Outline each blood parasite and name the species.
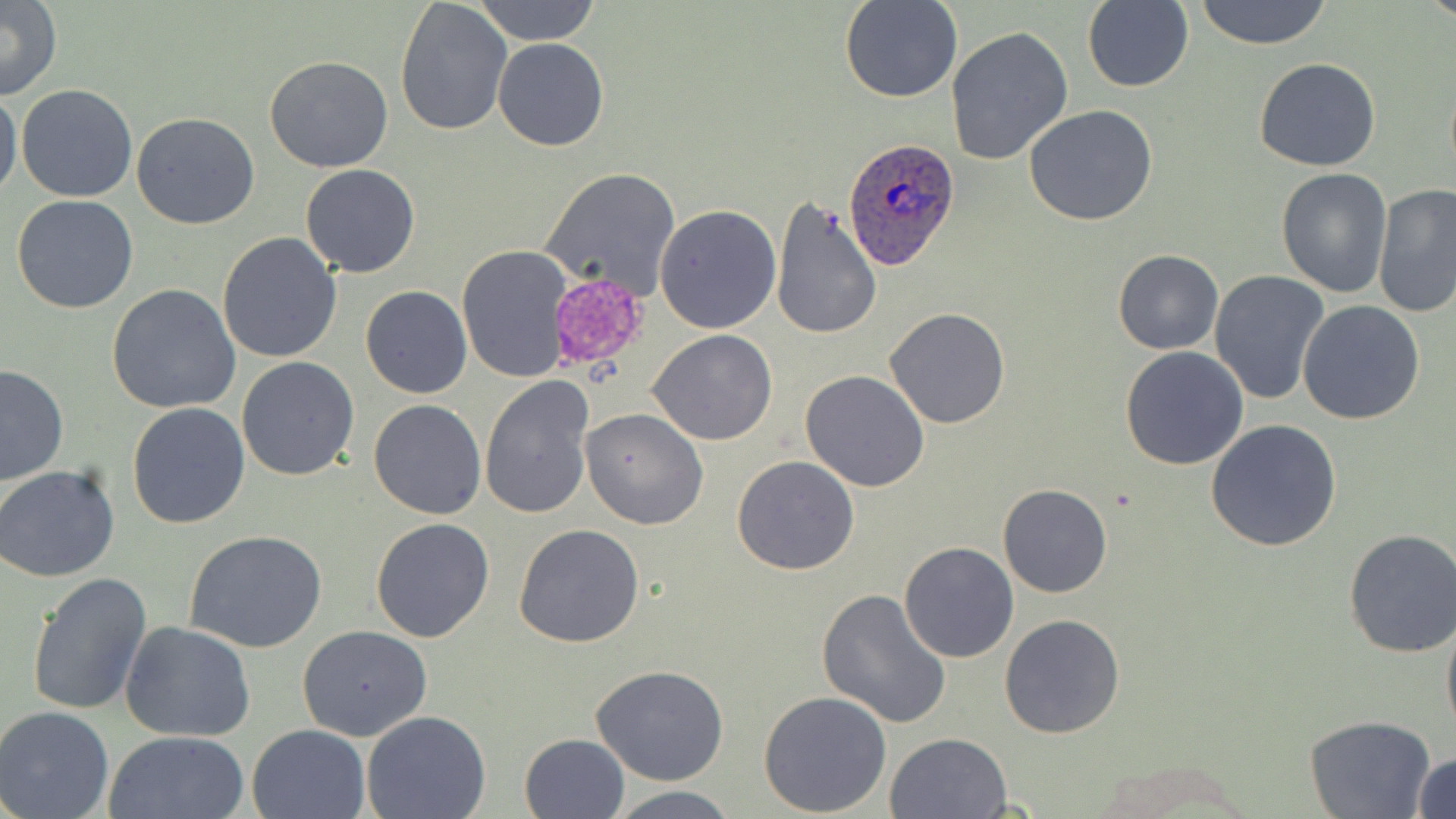

Approximate bounding boxes as (x1, y1, x2, y2) in pixels.
Plasmodium ovale-infected red blood cells: (844, 139, 959, 272).
No Plasmodium falciparum, Plasmodium malariae, Plasmodium vivax, Babesia divergens, or Trypanosoma brucei observed.

slide-level diagnosis = Plasmodium ovale
preparation = thin blood smear
modality = optical microscopy
image size = 1456×819 pixels
uninfected red blood cell locations = approximate bounding boxes as (x1, y1, x2, y2) in pixels: (473, 0, 602, 46), (839, 0, 962, 103), (1193, 0, 1333, 49), (0, 1, 62, 100), (393, 1, 512, 137), (1082, 1, 1195, 93), (946, 25, 1074, 167), (492, 38, 609, 151), (263, 55, 395, 173), (1254, 57, 1382, 171), (15, 84, 139, 203), (0, 86, 23, 203), (1023, 105, 1159, 227), (132, 112, 259, 229), (298, 165, 420, 279), (540, 167, 679, 300), (1276, 167, 1392, 297), (1372, 184, 1456, 318), (11, 194, 140, 315), (769, 196, 882, 341), (655, 204, 782, 334), (217, 232, 343, 363), (457, 245, 572, 383), (1112, 250, 1223, 356), (1208, 269, 1331, 409), (107, 285, 241, 414), (359, 285, 472, 397), (1298, 300, 1425, 425), (883, 308, 1012, 429), (648, 329, 777, 446), (1119, 346, 1249, 469), (236, 357, 361, 481), (0, 364, 70, 487), (800, 370, 930, 493), (480, 377, 597, 522), (368, 399, 487, 519), (127, 402, 250, 530), (580, 409, 709, 530), (1206, 419, 1342, 553), (731, 454, 859, 575), (0, 465, 121, 582), (998, 483, 1112, 598), (370, 518, 495, 643), (512, 524, 644, 648), (182, 529, 328, 653), (1343, 529, 1456, 657), (898, 541, 1019, 663), (26, 572, 152, 717), (816, 588, 952, 729), (999, 613, 1127, 739), (1441, 615, 1456, 743), (121, 620, 256, 741), (296, 624, 433, 742), (590, 664, 730, 786), (757, 689, 892, 815), (0, 706, 117, 819), (361, 711, 491, 819), (1304, 714, 1435, 819), (246, 724, 370, 819), (103, 730, 248, 819), (885, 731, 1013, 819), (519, 733, 630, 819), (1411, 751, 1455, 819), (605, 784, 742, 818)
field of view = single
magnification = 1000x
platelet locations = approximate bounding boxes as (x1, y1, x2, y2) in pixels: (545, 271, 651, 376)
stain = May-Grünwald-Giemsa